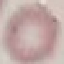

Result: no malaria parasites detected. Cell patch, automatically extracted from a larger field of view and resized to 64 × 64 pixels. Photographed with a smartphone camera at the microscope eyepiece. Thin blood film. Giemsa-stained preparation.